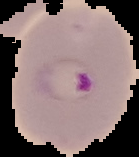

preparation = thin blood smear
malaria status = parasitized
image size = 139×157 pixels
image type = segmented cell region on a black background